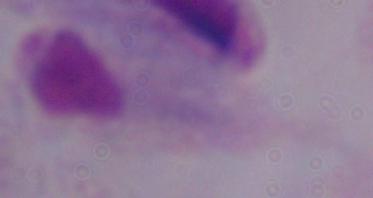
{
  "magnification": "1000x",
  "modality": "micrograph",
  "identification": "trichomonad"
}